Give the extent of all uninfected red blood cells.
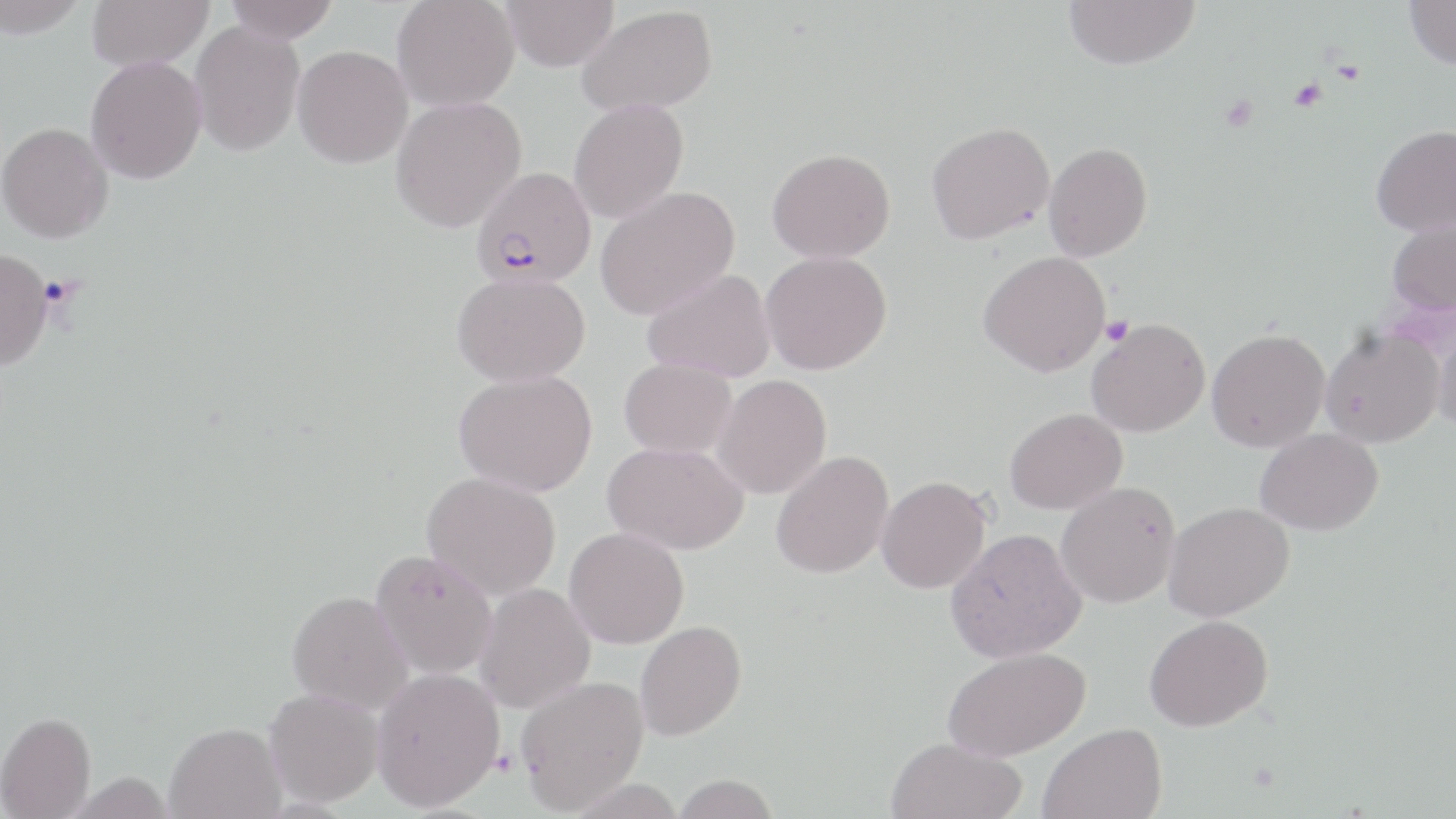
Approximate bounding boxes as (x1, y1, x2, y2) in pixels.
Uninfected red blood cells: (0, 0, 89, 39), (86, 0, 214, 72), (224, 0, 339, 44), (391, 0, 519, 112), (500, 0, 619, 71), (1063, 0, 1200, 70), (1404, 0, 1456, 70), (577, 5, 717, 116), (189, 21, 305, 157), (292, 45, 413, 168), (85, 56, 207, 184), (390, 95, 527, 233), (568, 98, 688, 223), (926, 121, 1054, 245), (1, 122, 114, 243), (1371, 124, 1456, 236), (1043, 142, 1152, 262), (767, 148, 896, 263), (594, 185, 740, 320), (1387, 217, 1456, 316), (0, 248, 53, 372), (760, 250, 892, 375), (977, 250, 1111, 377), (642, 268, 776, 383), (452, 271, 590, 387), (1430, 313, 1456, 437), (1086, 318, 1210, 437), (1319, 327, 1443, 448), (1206, 328, 1330, 452), (619, 357, 737, 459), (453, 369, 597, 496), (712, 374, 832, 499), (1004, 408, 1127, 514), (1255, 428, 1383, 536), (602, 441, 749, 555), (770, 450, 894, 579), (422, 471, 561, 601), (876, 475, 992, 594), (1055, 481, 1181, 608), (1163, 501, 1295, 622), (564, 527, 689, 649), (945, 528, 1087, 663), (370, 549, 498, 679), (474, 583, 595, 713), (287, 590, 413, 714), (1143, 615, 1273, 732), (635, 620, 747, 741), (941, 646, 1090, 762), (371, 667, 505, 811), (516, 675, 649, 814), (264, 687, 384, 807), (0, 712, 95, 818), (164, 721, 286, 818), (1039, 722, 1166, 818), (885, 737, 1027, 819), (672, 774, 780, 818).

Platelet locations: (1289, 78, 1328, 111), (1219, 94, 1259, 132), (1101, 316, 1133, 346). Plasmodium falciparum-infected red blood cell locations: (471, 166, 596, 288). Slide-level diagnosis: Plasmodium falciparum. Captured at 1000x magnification. Image is 1456×819 pixels. One field of a larger specimen. May-Grünwald-Giemsa stain. Thin blood film. Optical microscopy.